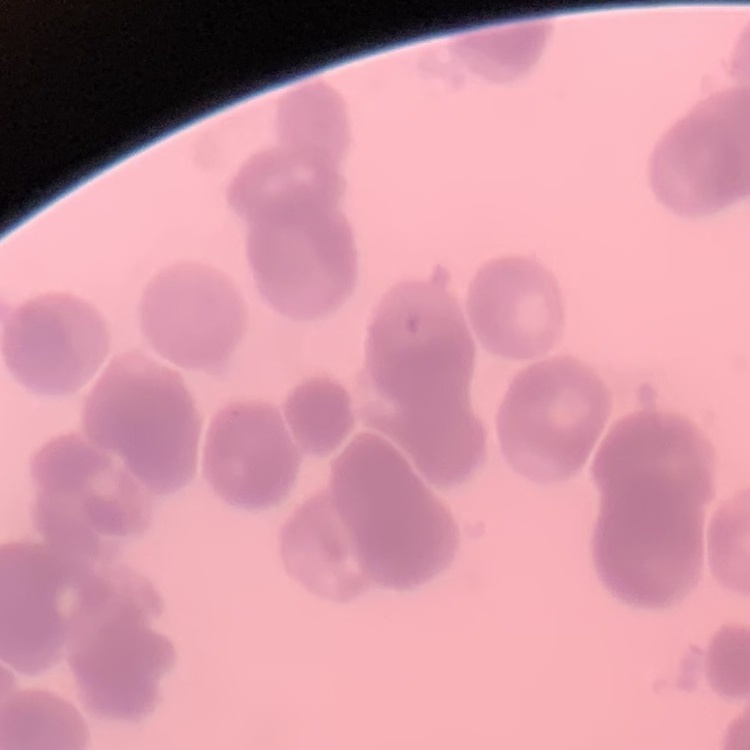 The red blood cells show rouleaux formation. Thin blood smear. One tile cut from a larger photomicrograph. Stained with either Field's or Giemsa.